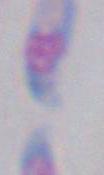

Photomicrograph. Captured at 1000x magnification. Toxoplasma gondii is shown.